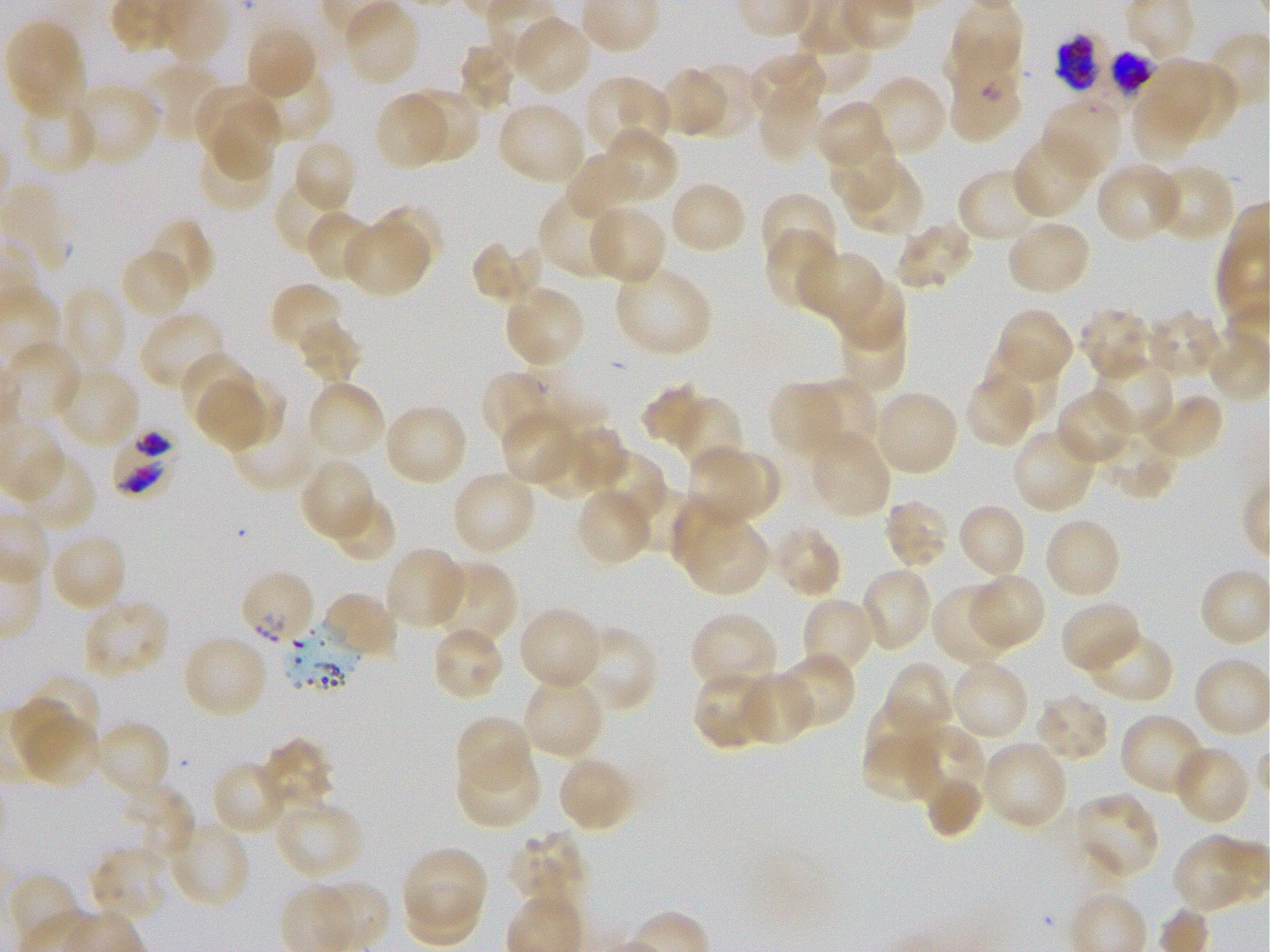
Approximate bounding boxes as {x1, y1, x2, y2} in pixels. Not every red blood cell is marked. A life-cycle stage — or a range of stages, where the recorded stages span more than one — follows each staged infected red blood cell. Locations of uninfected red blood cells: {342, 1, 421, 86}, {513, 16, 592, 96}, {5, 20, 86, 115}, {794, 22, 872, 94}, {244, 23, 316, 100}, {456, 42, 518, 114}, {747, 51, 827, 122}, {1133, 59, 1211, 163}, {142, 62, 224, 142}, {692, 64, 759, 139}, {253, 66, 335, 144}, {1166, 66, 1237, 140}, {658, 68, 728, 139}, {584, 74, 671, 158}, {868, 75, 947, 158}, {70, 83, 160, 167}, {195, 84, 270, 148}, {405, 88, 479, 163}, {757, 90, 824, 162}, {20, 93, 98, 176}, {374, 93, 448, 171}, {212, 95, 284, 178}, {1042, 97, 1123, 179}, {814, 101, 892, 173}, {497, 103, 587, 185}, {601, 128, 679, 203}, {829, 129, 897, 211}, {1012, 134, 1093, 219}, {195, 135, 274, 214}, {291, 139, 357, 214}, {563, 154, 641, 216}, {841, 156, 923, 235}, {1095, 162, 1182, 243}, {1152, 163, 1236, 244}, {958, 167, 1048, 245}, {275, 177, 348, 255}, {669, 181, 749, 255}, {539, 190, 622, 279}, {759, 192, 838, 267}, {369, 204, 443, 275}, {586, 205, 667, 286}, {306, 210, 377, 282}, {145, 218, 216, 293}, {1005, 220, 1092, 296}, {894, 221, 976, 291}, {344, 222, 429, 297}, {763, 228, 836, 310}, {470, 239, 540, 307}, {120, 248, 194, 320}, {798, 250, 885, 327}, {614, 263, 711, 357}, {839, 275, 904, 353}, {268, 282, 343, 355}, {59, 286, 127, 372}, {503, 286, 586, 368}, {997, 308, 1074, 384}, {1078, 308, 1155, 382}, {1148, 309, 1223, 378}, {141, 310, 227, 391}, {837, 313, 906, 395}, {296, 318, 363, 384}, {5, 341, 83, 422}, {179, 350, 255, 428}, {988, 352, 1063, 425}, {1091, 360, 1175, 436}, {55, 366, 139, 450}, {481, 371, 545, 447}, {964, 371, 1037, 449}, {218, 374, 287, 445}, {802, 377, 880, 457}, {199, 378, 265, 452}, {306, 380, 386, 460}, {768, 381, 843, 460}, {641, 383, 708, 449}, {1055, 388, 1135, 467}, {873, 389, 959, 476}, {1144, 393, 1225, 462}, {670, 396, 742, 473}, {384, 402, 469, 486}, {500, 412, 579, 487}, {230, 415, 318, 492}, {568, 424, 631, 490}, {1011, 426, 1093, 517}, {1098, 428, 1179, 500}, {807, 431, 892, 519}, {542, 435, 598, 500}, {689, 445, 760, 523}, {590, 450, 668, 529}, {717, 450, 782, 515}, {16, 452, 97, 532}, {300, 459, 375, 542}, {450, 470, 537, 556}, {627, 484, 698, 553}, {575, 487, 653, 567}, {670, 493, 739, 571}, {327, 496, 397, 564}, {883, 499, 952, 570}, {956, 503, 1027, 580}, {683, 514, 769, 596}, {1043, 516, 1123, 599}, {771, 524, 843, 599}, {49, 534, 127, 614}, {383, 547, 466, 630}, {431, 561, 518, 648}, {858, 566, 933, 652}, {971, 573, 1047, 650}, {931, 584, 1014, 666}, {322, 592, 399, 660}, {801, 596, 878, 678}, {81, 598, 171, 679}, {1060, 599, 1142, 675}, {517, 605, 603, 691}, {689, 612, 779, 693}, {574, 624, 659, 715}, {431, 627, 506, 701}, {1085, 629, 1175, 704}, {181, 634, 269, 719}, {519, 639, 604, 728}, {776, 651, 856, 729}, {949, 658, 1030, 740}, {882, 661, 955, 740}, {693, 669, 771, 750}, {737, 670, 816, 746}, {24, 674, 101, 752}, {520, 676, 604, 759}, {1034, 692, 1111, 764}, {8, 698, 81, 772}, {864, 701, 947, 776}, {1120, 713, 1207, 797}, {22, 714, 102, 790}, {454, 715, 535, 793}, {95, 719, 171, 799}, {903, 724, 984, 808}, {861, 732, 940, 798}, {259, 737, 335, 814}, {982, 739, 1069, 831}, {1171, 744, 1251, 825}, {455, 751, 542, 830}, {558, 754, 636, 833}, {211, 759, 289, 836}, {924, 773, 982, 839}, {122, 782, 195, 863}, {1074, 791, 1161, 881}, {274, 801, 364, 881}, {166, 822, 251, 908}, {505, 832, 588, 909}, {1172, 834, 1252, 910}, {89, 846, 169, 924}, {402, 846, 487, 925}, {403, 880, 481, 946}. Locations of infected red blood cells: {948, 38, 1025, 142} early ring; {1108, 48, 1154, 95} late trophozoite to late schizont; {113, 428, 178, 498}. Locations of red blood cells of indeterminate infection status: {1055, 33, 1101, 94}, {243, 571, 313, 646}. Blood group of the donor: O+. 100x objective under oil immersion, numerical aperture 1.25. Image is 1270×952 pixels. Thin blood film. Plasmodium falciparum strain 3D7 maintained in static in-vitro culture. Giemsa stain. One field from this slide.